Report the malaria status of this cell.
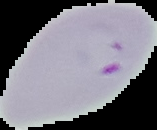
It is parasitized.

image type = segmented cell region on a black background
preparation = thin blood smear
image size = 157×130 pixels